Assess this cell for malaria.
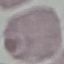

Uninfected.

image type = cell patch, automatically extracted from a larger field of view and resized to 64 × 64 pixels
preparation = thin smear
stain = Giemsa
capture = smartphone camera at the microscope eyepiece